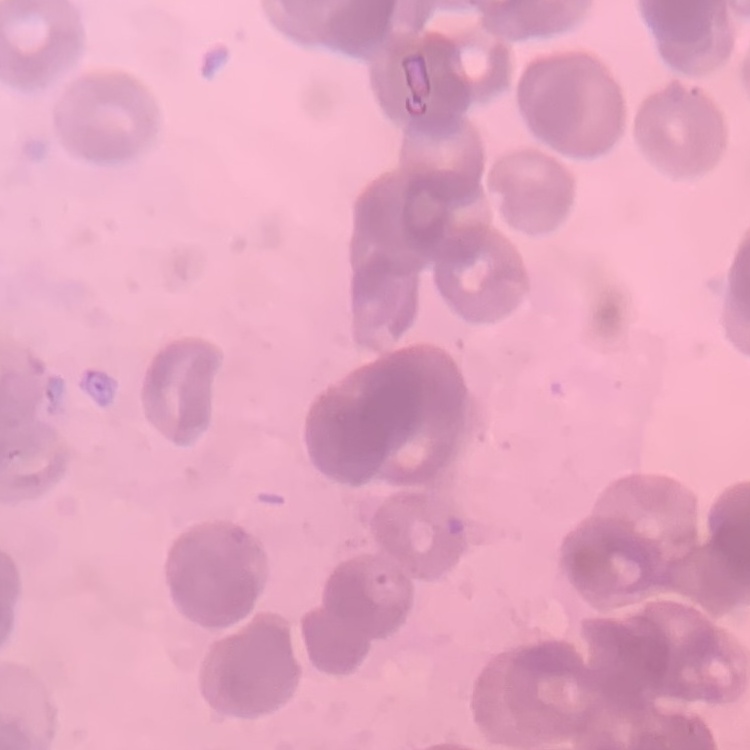
Summary:
  - Erythrocyte morphology: rouleaux formation
  - Stain: Field's or Giemsa
  - Preparation: thin blood smear
  - Image type: one tile cut from a larger photomicrograph